Describe the morphology of the red blood cells.
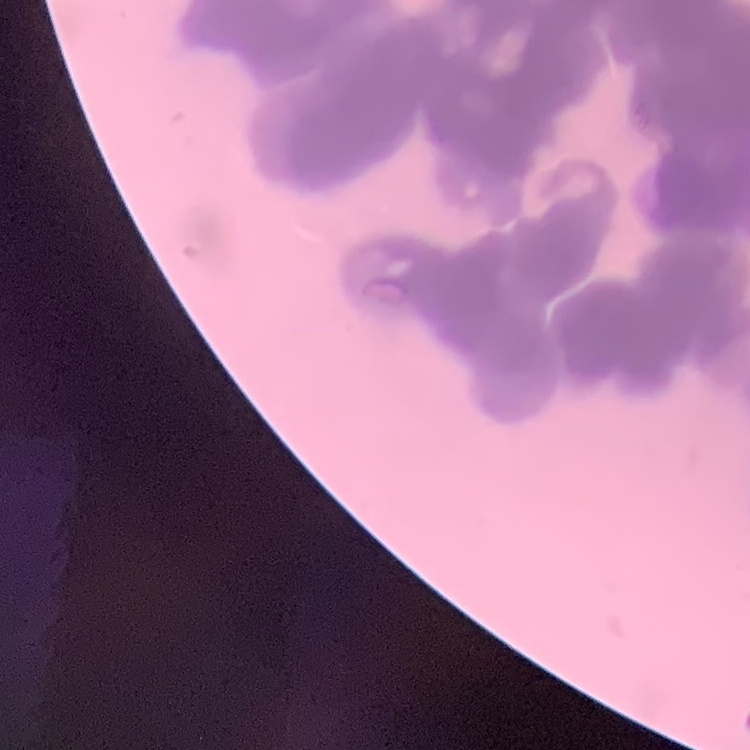
Rouleaux formation.

preparation: thin blood film
image_type: one tile cut from a larger photomicrograph
stain: Field's or Giemsa